Assess for malaria.
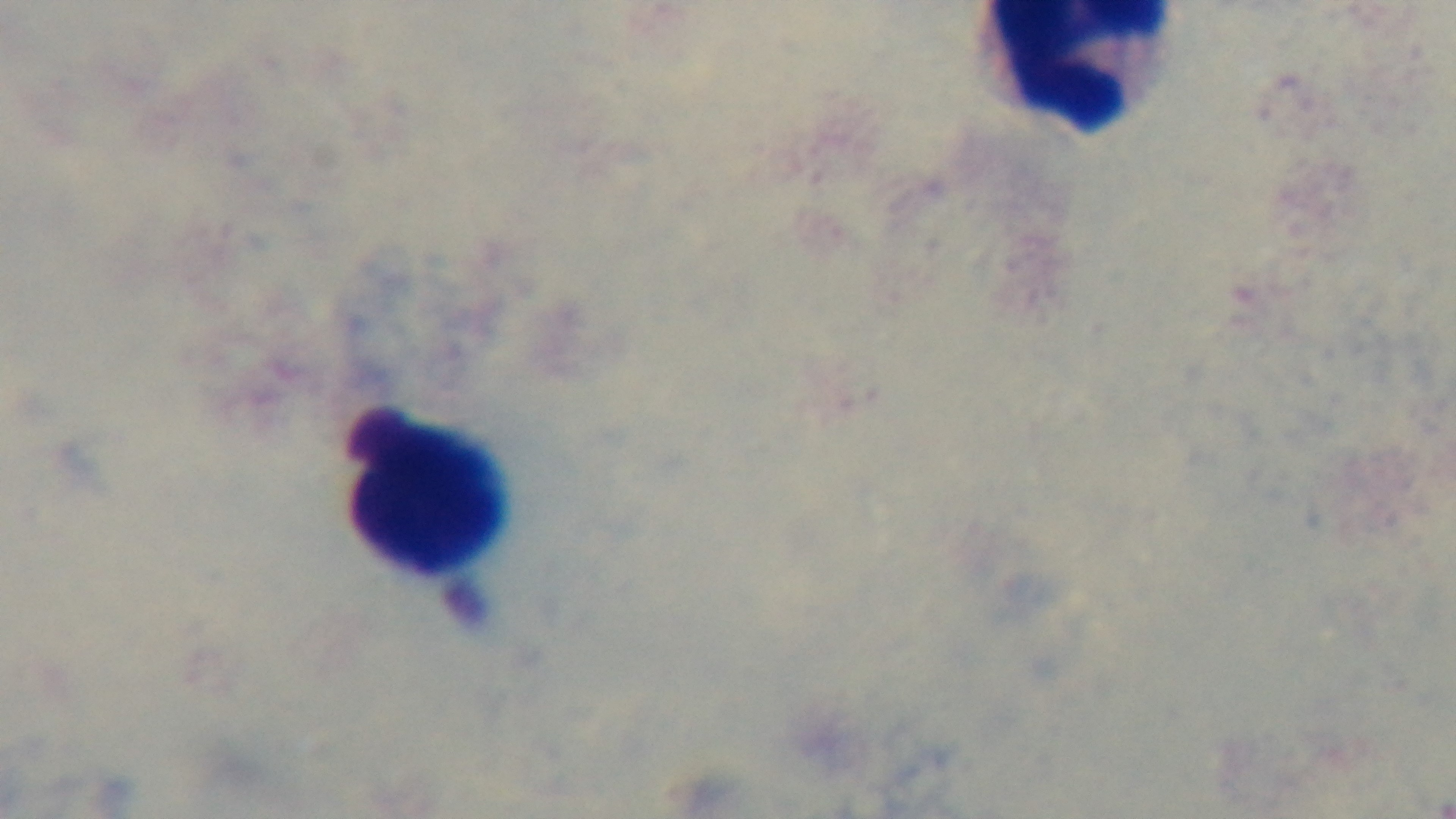
Uninfected.

Summary:
  - Field of view: single
  - Modality: light microscopy
  - Objective: 100x oil immersion
  - Preparation: thick
  - Stain: Giemsa
  - Capture: mounted 4K digital camera